Name the cell type shown.
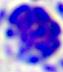

A leukocyte.

magnification = 400x
modality = photomicrograph